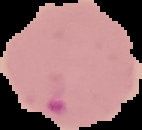

Summary:
  - Image size: 142×130 pixels
  - Result: Plasmodium parasites detected
  - Image type: segmented cell region on a black background
  - Preparation: thin blood smear